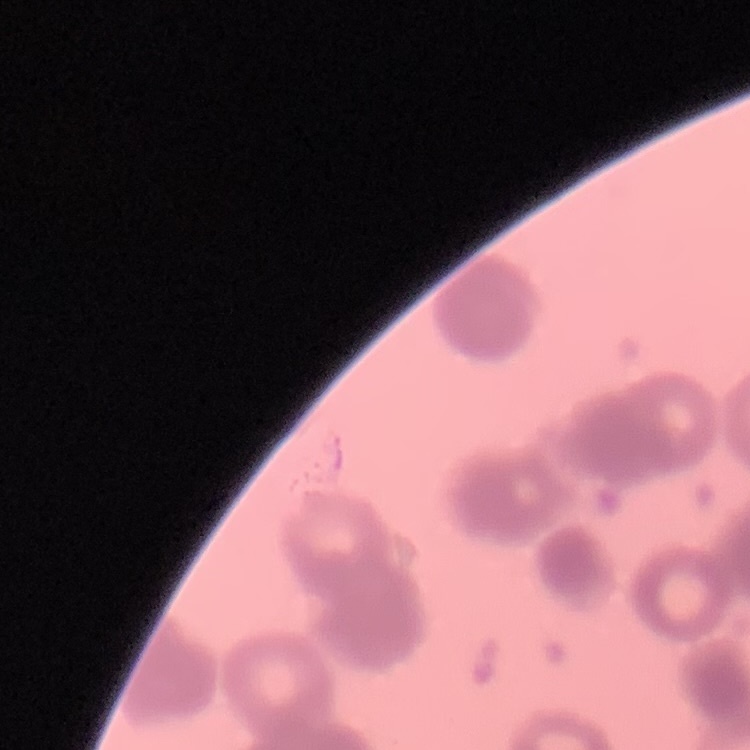
red blood cell morphology = rouleaux formation
image type = one tile cut from a larger photomicrograph
stain = Field's or Giemsa
preparation = thin blood film